Outline each blood parasite and name the species.
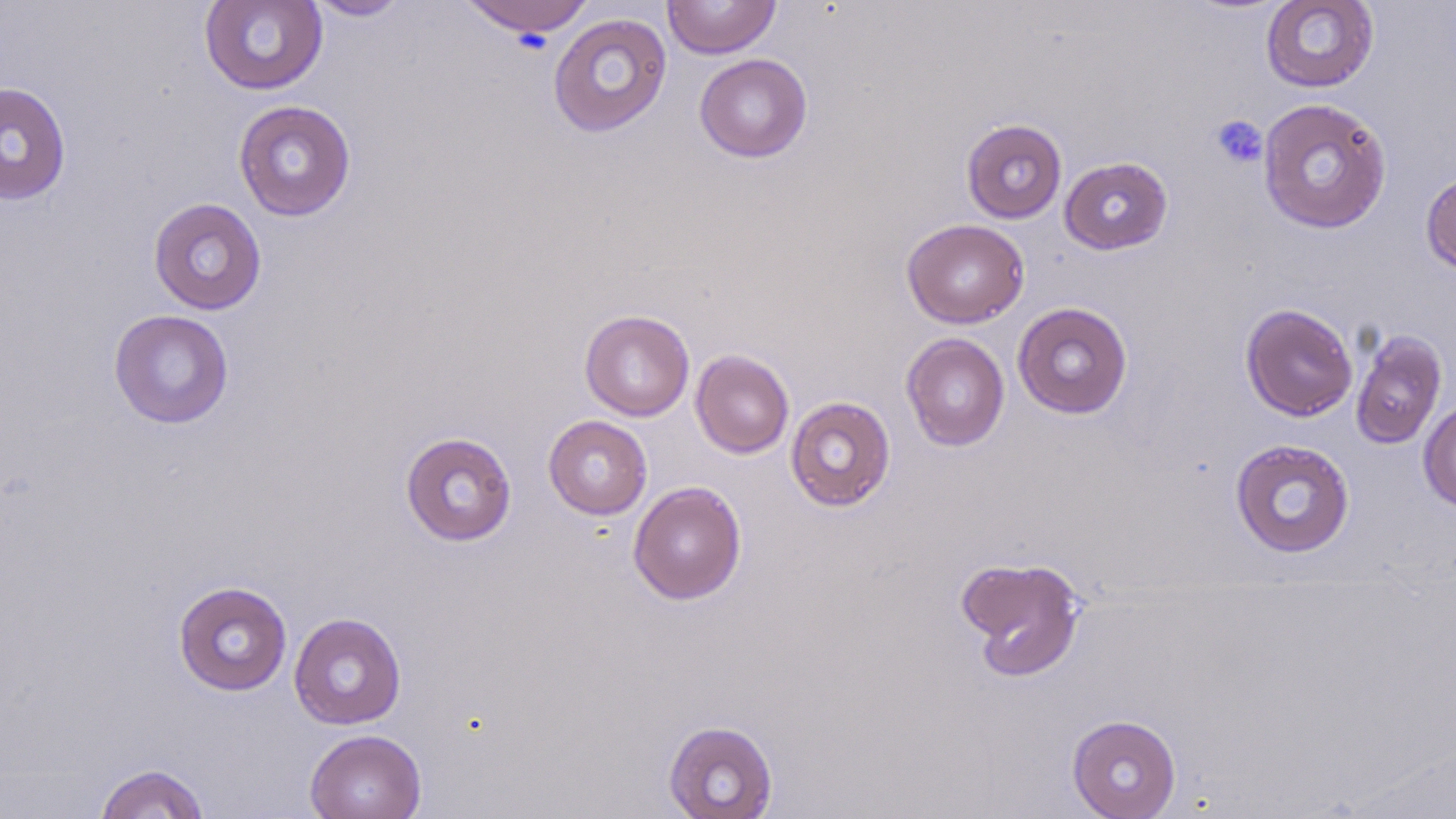
No blood parasites seen.

Summary:
  - Coordinate format: approximate bounding boxes as (x1,y1)-(x2,y2) corner pairs in pixels
  - Uninfected red blood cell locations: (199,0)-(328,95), (302,0)-(412,21), (459,0)-(595,38), (663,0)-(780,59), (1260,0)-(1379,93), (548,13)-(672,137), (695,54)-(813,163), (0,81)-(71,206), (1257,97)-(1393,234), (233,100)-(357,222), (961,118)-(1067,224), (1060,156)-(1173,255), (1420,171)-(1456,276), (148,197)-(267,315), (902,218)-(1029,328), (1012,302)-(1133,419), (1241,303)-(1358,422), (108,309)-(234,429), (579,309)-(695,421), (1350,328)-(1448,450), (900,332)-(1010,451), (691,350)-(794,459), (786,395)-(896,511), (1418,398)-(1456,513), (543,415)-(652,520), (400,431)-(517,546), (1230,439)-(1355,558), (628,480)-(746,605), (955,555)-(1086,681), (173,580)-(292,696), (289,612)-(406,730), (1066,714)-(1181,819), (663,720)-(778,819), (305,728)-(427,819), (93,762)-(211,818)
  - Platelet locations: (1209,114)-(1268,169)
  - Slide-level diagnosis: negative for blood parasites
  - Stain: May-Grünwald-Giemsa
  - Magnification: 1000x
  - Image size: 1456×819 pixels
  - Modality: light microscopy
  - Field of view: one of a larger specimen
  - Preparation: thin blood smear